Assess the morphology of the red blood cells.
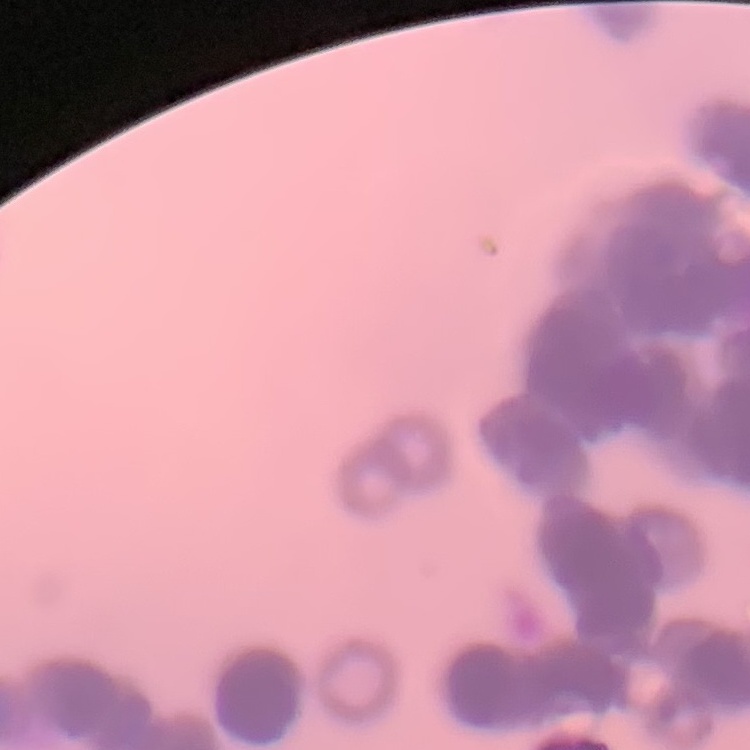
They show rouleaux formation.

Thin blood smear. One tile cut from a larger photomicrograph. Stained with either Field's or Giemsa.